State which parasite is depicted.
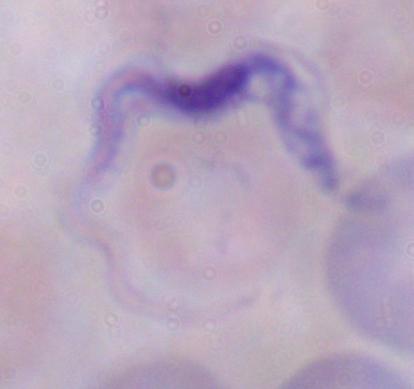
This is a trypanosome.

Micrograph. 1000x magnification.